Comment on the morphology of the red blood cells.
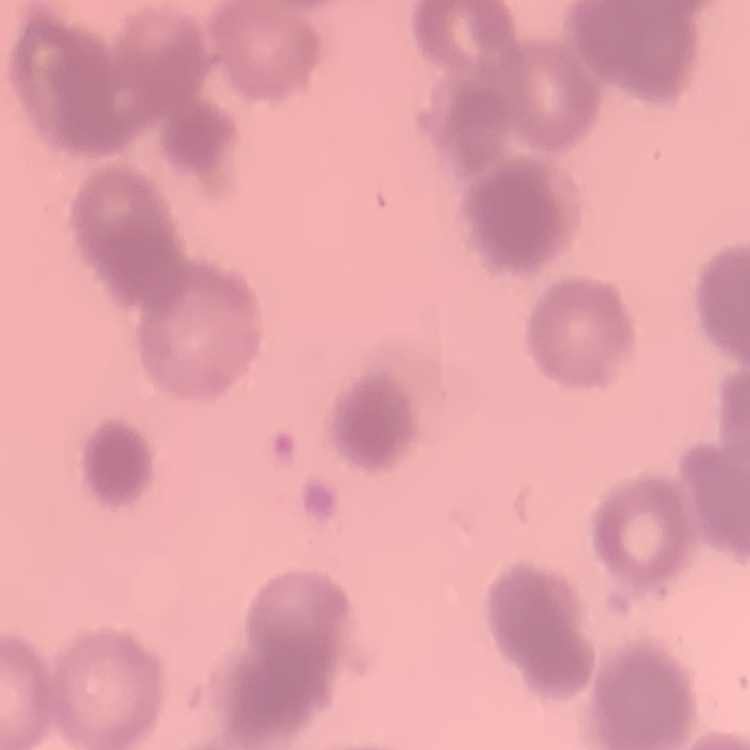

They show rouleaux formation.

Summary:
  - Image type: one tile cut from a larger photomicrograph
  - Preparation: thin peripheral smear
  - Stain: Field's or Giemsa